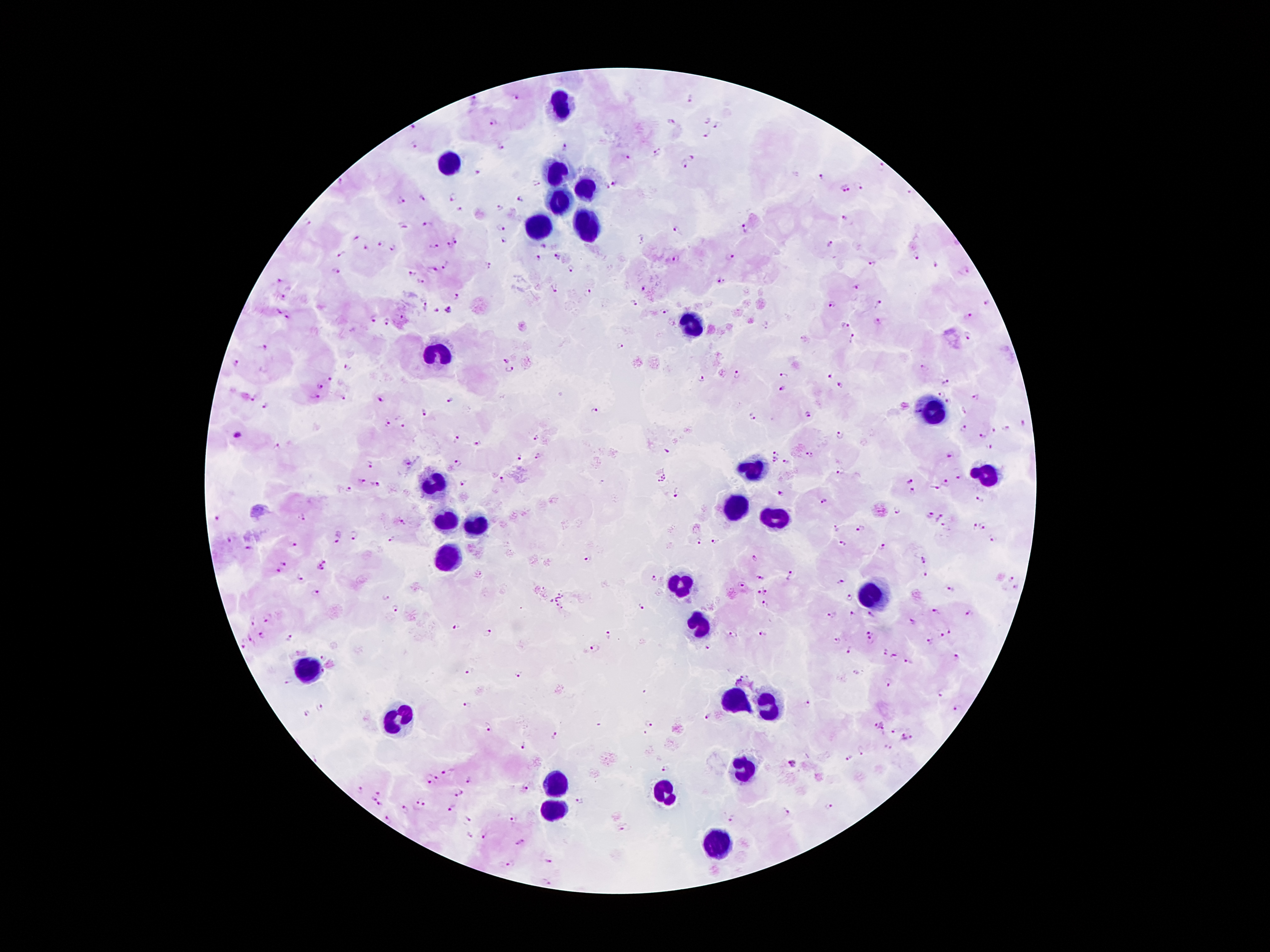

Approximate object centers, in pixels from the top-left corner.
Summary:
  - Leukocyte locations: (x=559, y=105), (x=450, y=164), (x=555, y=176), (x=585, y=187), (x=559, y=204), (x=536, y=229), (x=585, y=229), (x=690, y=329), (x=433, y=351), (x=933, y=411), (x=753, y=468), (x=988, y=478), (x=435, y=485), (x=734, y=509), (x=778, y=518), (x=446, y=521), (x=471, y=523), (x=450, y=562), (x=677, y=586), (x=872, y=598), (x=698, y=626), (x=305, y=668), (x=734, y=701), (x=767, y=706), (x=393, y=721), (x=744, y=773), (x=555, y=786), (x=660, y=791), (x=553, y=812), (x=717, y=847)
  - Malaria parasite locations: (x=516, y=96), (x=474, y=99), (x=689, y=100), (x=706, y=120), (x=670, y=121), (x=493, y=124), (x=412, y=128), (x=716, y=128), (x=705, y=135), (x=413, y=146), (x=500, y=146), (x=564, y=150), (x=658, y=153), (x=693, y=157), (x=628, y=158), (x=684, y=166), (x=881, y=167), (x=478, y=173), (x=822, y=175), (x=340, y=180), (x=534, y=181), (x=613, y=183), (x=858, y=185), (x=845, y=187), (x=909, y=193), (x=452, y=196), (x=420, y=199), (x=520, y=199), (x=402, y=200), (x=500, y=208), (x=459, y=209), (x=845, y=218), (x=307, y=223), (x=429, y=225), (x=401, y=226), (x=501, y=228), (x=745, y=228), (x=677, y=229), (x=355, y=237), (x=502, y=239), (x=379, y=243), (x=451, y=243), (x=828, y=243), (x=433, y=245), (x=544, y=245), (x=365, y=249), (x=392, y=249), (x=340, y=255), (x=558, y=255), (x=538, y=257), (x=916, y=257), (x=677, y=259), (x=731, y=259), (x=489, y=264), (x=871, y=264), (x=447, y=266), (x=934, y=267), (x=572, y=269), (x=434, y=270), (x=337, y=272), (x=412, y=272), (x=968, y=272), (x=279, y=279), (x=419, y=282), (x=721, y=282), (x=555, y=288), (x=855, y=288), (x=643, y=289), (x=586, y=293), (x=282, y=295), (x=456, y=296), (x=633, y=303), (x=879, y=303), (x=986, y=303), (x=832, y=305), (x=424, y=308), (x=449, y=308), (x=278, y=310), (x=435, y=311), (x=661, y=312), (x=968, y=315), (x=286, y=318), (x=373, y=319), (x=878, y=321), (x=387, y=322), (x=845, y=325), (x=968, y=333), (x=853, y=339), (x=619, y=343), (x=264, y=350), (x=504, y=360), (x=236, y=364), (x=346, y=367), (x=925, y=368), (x=510, y=371), (x=738, y=372), (x=784, y=377), (x=830, y=377), (x=699, y=379), (x=329, y=381), (x=947, y=384), (x=319, y=385), (x=841, y=386), (x=783, y=389), (x=941, y=395), (x=254, y=396), (x=314, y=397), (x=976, y=397), (x=342, y=399), (x=450, y=399), (x=380, y=400), (x=949, y=401), (x=266, y=406), (x=594, y=411), (x=963, y=411), (x=425, y=412), (x=808, y=414), (x=751, y=417), (x=386, y=421), (x=1023, y=424), (x=402, y=427), (x=963, y=429), (x=1009, y=429), (x=994, y=431), (x=840, y=434), (x=238, y=435), (x=982, y=436), (x=536, y=437), (x=458, y=438), (x=475, y=443), (x=276, y=446), (x=990, y=447), (x=775, y=452), (x=534, y=455), (x=950, y=455), (x=522, y=456), (x=810, y=456), (x=776, y=460), (x=786, y=461), (x=408, y=463), (x=459, y=463), (x=368, y=464), (x=840, y=472), (x=959, y=477), (x=361, y=480), (x=500, y=480), (x=910, y=481), (x=945, y=483), (x=375, y=485), (x=461, y=485), (x=935, y=487), (x=348, y=489), (x=912, y=490), (x=781, y=492), (x=677, y=493), (x=980, y=501), (x=825, y=502), (x=896, y=511), (x=304, y=516), (x=930, y=516), (x=938, y=517), (x=217, y=520), (x=402, y=521), (x=983, y=526), (x=945, y=527), (x=974, y=527), (x=860, y=529), (x=836, y=530), (x=352, y=533), (x=337, y=535), (x=389, y=538), (x=228, y=539), (x=992, y=540), (x=699, y=542), (x=717, y=542), (x=293, y=544), (x=842, y=544), (x=882, y=548), (x=249, y=549), (x=587, y=558), (x=754, y=558), (x=924, y=560), (x=283, y=563), (x=325, y=565), (x=276, y=572), (x=926, y=575), (x=791, y=576), (x=300, y=577), (x=655, y=578), (x=762, y=578), (x=1012, y=579), (x=842, y=582), (x=742, y=585), (x=951, y=587), (x=1015, y=588), (x=765, y=591), (x=318, y=592), (x=758, y=593), (x=384, y=597), (x=850, y=599), (x=765, y=604), (x=640, y=606), (x=395, y=608), (x=937, y=611), (x=969, y=613), (x=832, y=614), (x=852, y=614), (x=871, y=614), (x=266, y=619), (x=253, y=622), (x=912, y=622), (x=457, y=626), (x=870, y=631), (x=950, y=631), (x=489, y=632), (x=734, y=634), (x=764, y=634), (x=262, y=635), (x=608, y=635), (x=943, y=636), (x=289, y=637), (x=249, y=639), (x=836, y=640), (x=870, y=641), (x=930, y=641), (x=244, y=645), (x=711, y=647), (x=595, y=649), (x=849, y=650), (x=887, y=651), (x=895, y=654), (x=323, y=656), (x=955, y=656), (x=909, y=662), (x=470, y=671), (x=323, y=673), (x=518, y=675), (x=286, y=681), (x=888, y=682), (x=940, y=693), (x=467, y=703), (x=810, y=704), (x=320, y=706), (x=956, y=709), (x=307, y=712), (x=708, y=716), (x=648, y=724), (x=880, y=724), (x=489, y=726), (x=891, y=730), (x=644, y=734), (x=556, y=736), (x=903, y=736), (x=910, y=737), (x=525, y=746), (x=887, y=746), (x=862, y=750), (x=849, y=758), (x=792, y=763), (x=665, y=771), (x=447, y=772), (x=437, y=778), (x=427, y=779), (x=468, y=779), (x=525, y=789), (x=361, y=790), (x=377, y=793), (x=459, y=793), (x=372, y=799), (x=421, y=800), (x=580, y=800), (x=380, y=803), (x=830, y=807), (x=405, y=809), (x=451, y=809), (x=784, y=812), (x=512, y=819), (x=731, y=819), (x=469, y=820), (x=389, y=821), (x=621, y=829), (x=470, y=837), (x=484, y=837), (x=521, y=843), (x=550, y=857), (x=510, y=864)
  - Image size: 1270×952 pixels
  - Field of view: one from this slide
  - Capture: smartphone through the microscope eyepiece
  - Stain: Giemsa
  - Preparation: thick blood smear
  - Patient malaria status: positive for Plasmodium falciparum
  - Magnification: 100x